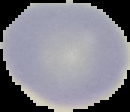 From a thin blood film. Malaria status: uninfected. Image is 130×112 pixels. Cell region segmented out of the field of view; the surrounding area is masked to black.